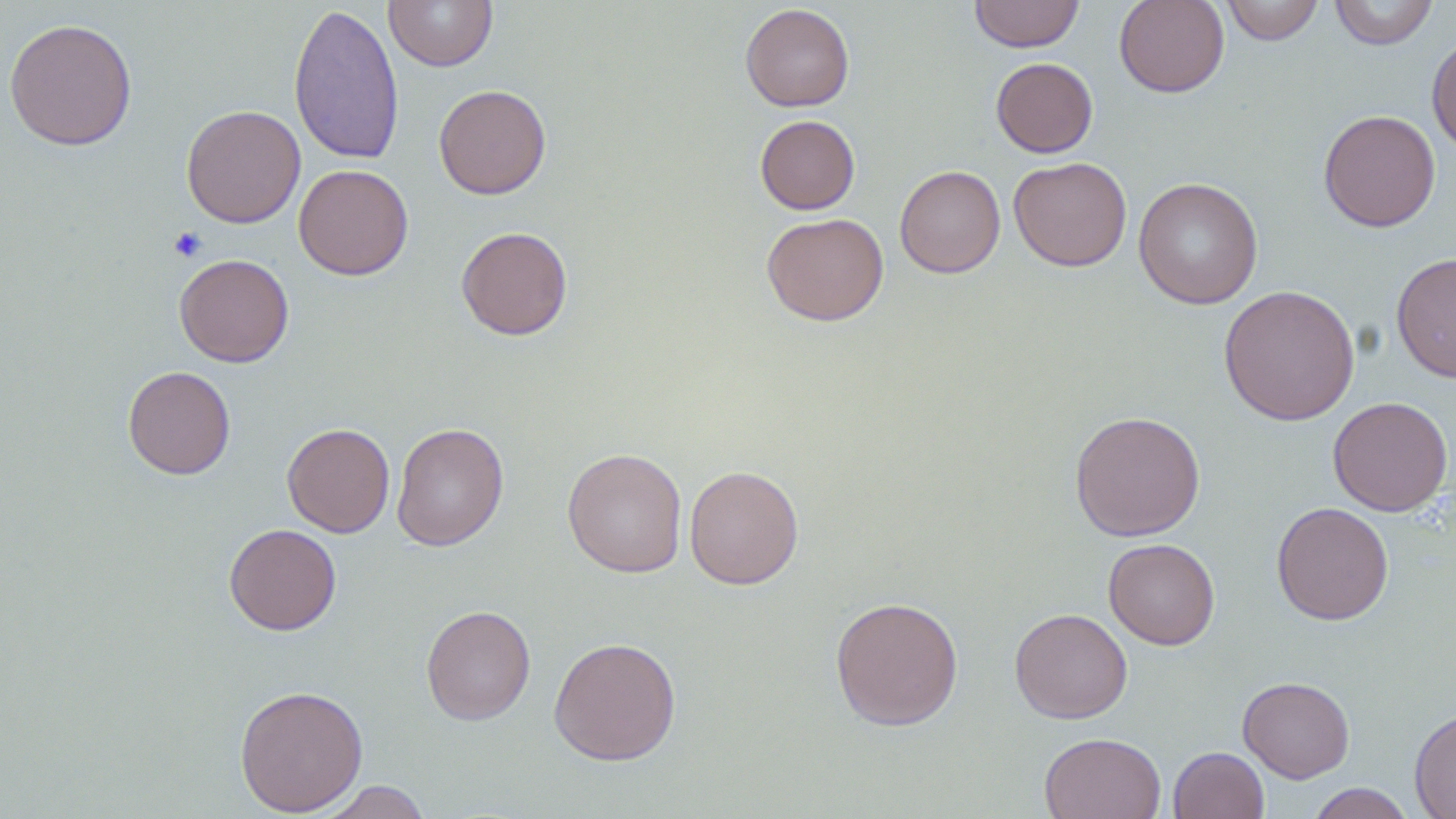
{
  "slide_level_diagnosis": "no evidence of blood parasites",
  "image_size": "1456×819 pixels",
  "magnification": "1000x",
  "field_of_view": "one of a larger specimen",
  "uninfected_red_blood_cell_locations": "approximate bounding boxes as (x1, y1, x2, y2) in pixels: (383, 0, 499, 72), (969, 0, 1085, 52), (1114, 0, 1229, 98), (1220, 0, 1325, 45), (1328, 0, 1439, 50), (288, 3, 405, 166), (740, 4, 855, 111), (3, 17, 138, 151), (1426, 34, 1456, 155), (991, 57, 1098, 158), (433, 84, 551, 199), (181, 104, 306, 228), (1318, 110, 1441, 232), (755, 114, 860, 214), (1008, 156, 1132, 272), (294, 163, 414, 280), (895, 165, 1005, 278), (1133, 177, 1264, 309), (761, 212, 889, 326), (456, 226, 573, 340), (1390, 252, 1456, 383), (174, 253, 294, 367), (1218, 284, 1360, 426), (123, 365, 236, 480), (1327, 396, 1453, 516), (1069, 409, 1205, 542), (391, 422, 509, 551), (282, 423, 395, 537), (562, 447, 688, 578), (684, 464, 804, 590), (1271, 502, 1395, 625), (224, 523, 341, 636), (1103, 538, 1220, 650), (829, 595, 964, 731), (420, 604, 536, 726), (1009, 607, 1132, 724), (549, 636, 682, 765), (1237, 675, 1355, 783), (234, 683, 368, 817), (1409, 707, 1456, 819), (1039, 732, 1166, 819), (1168, 745, 1269, 819), (315, 780, 434, 818), (1306, 783, 1416, 818)",
  "modality": "light microscopy",
  "preparation": "thin blood film",
  "stain": "May-Grünwald-Giemsa",
  "platelet_locations": "approximate bounding boxes as (x1, y1, x2, y2) in pixels: (168, 226, 207, 262)"
}